Mark where platelets are.
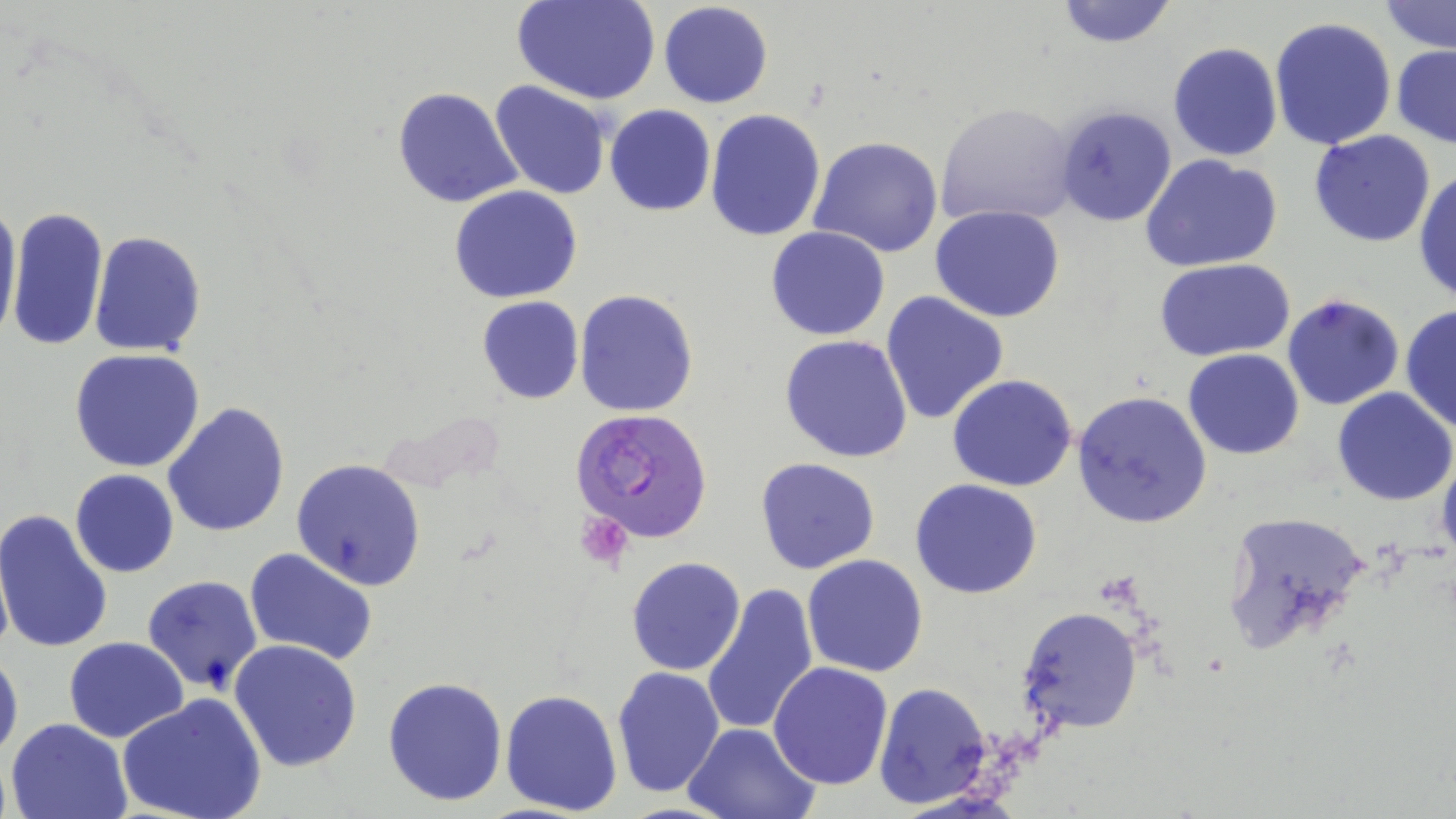

Approximate bounding boxes as (x1,y1)-(x2,y2) corner pairs in pixels.
Platelets: (575,511)-(632,568).

Plasmodium falciparum-infected red blood cell locations: (564,409)-(704,543). Uninfected red blood cell locations: (514,0)-(660,105), (1052,0)-(1181,49), (1379,1)-(1456,53), (657,2)-(773,109), (1268,16)-(1397,151), (1168,42)-(1283,163), (1391,44)-(1456,149), (490,81)-(611,200), (392,88)-(524,210), (936,102)-(1078,229), (605,105)-(715,216), (1054,105)-(1176,226), (704,108)-(827,242), (1308,129)-(1436,247), (810,136)-(945,259), (1141,154)-(1283,275), (1414,166)-(1456,304), (449,186)-(583,303), (0,197)-(21,345), (9,201)-(45,347), (930,205)-(1065,322), (7,209)-(108,349), (766,226)-(891,342), (89,229)-(206,356), (1154,258)-(1296,360), (574,289)-(698,417), (880,291)-(1010,428), (1280,293)-(1405,411), (477,296)-(583,404), (1400,306)-(1455,432), (779,333)-(913,463), (69,349)-(205,472), (1184,349)-(1305,459), (947,374)-(1079,492), (1332,388)-(1456,508), (1071,390)-(1212,527), (162,402)-(291,538), (1437,448)-(1456,562), (754,456)-(882,574), (290,457)-(427,590), (69,470)-(179,578), (909,479)-(1043,600), (0,508)-(116,656), (1223,509)-(1371,655), (244,547)-(379,667), (802,554)-(929,676), (626,556)-(746,676), (142,574)-(263,694), (700,582)-(816,737), (1018,607)-(1141,734), (64,637)-(188,743), (227,639)-(362,773), (0,645)-(23,766), (769,662)-(893,790), (611,666)-(725,798), (383,677)-(508,807), (873,681)-(993,809), (499,687)-(623,816), (118,694)-(266,819), (3,717)-(132,819), (683,721)-(822,819). Slide-level diagnosis: Plasmodium falciparum. Thin blood film. Image is 1456×819 pixels. May-Grünwald-Giemsa stain. One field of a larger specimen. Captured at 1000x magnification. Optical microscopy.